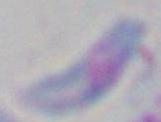

Summary:
  - Modality: micrograph
  - Identification: Toxoplasma gondii
  - Magnification: 1000x